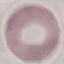

{
  "result": "negative for malaria parasites",
  "stain": "Giemsa",
  "preparation": "thin blood film",
  "capture": "smartphone camera at the microscope eyepiece",
  "image_type": "automatically extracted cell patch, resized to 64 × 64 pixels"
}